Draw a bounding box around every Plasmodium parasite.
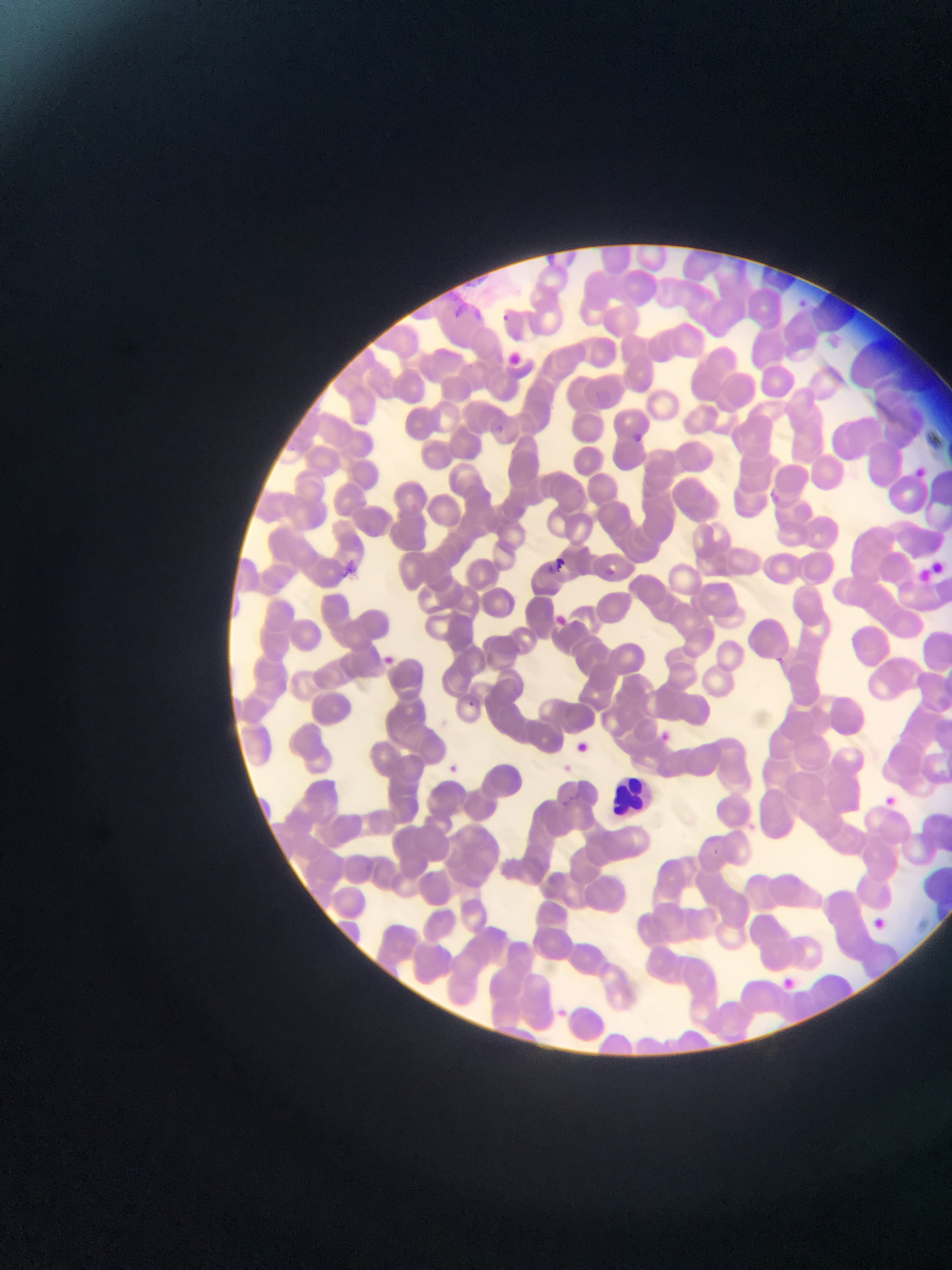

Approximate bounding boxes as (left, top, right, bottom) in pixels.
Plasmodium parasites: (794, 298, 810, 312), (793, 302, 811, 318), (494, 311, 515, 328), (490, 423, 509, 439), (625, 430, 649, 450), (910, 464, 930, 481), (765, 491, 784, 508), (545, 556, 572, 577), (607, 561, 622, 581), (552, 614, 571, 632), (378, 651, 397, 669), (463, 698, 485, 729), (656, 729, 674, 746), (573, 739, 592, 756), (442, 760, 463, 780), (557, 761, 575, 777), (881, 793, 898, 809), (706, 845, 724, 861), (862, 910, 891, 937), (771, 973, 797, 994).

Image is 952×1270 pixels. Collected in Ghana. One field of view. Thin blood film. Mobile-phone photograph taken through the microscope.